State which parasite is depicted.
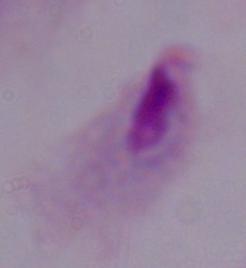
This is a trichomonad.

{
  "modality": "photomicrograph",
  "magnification": "1000x"
}